Locate every Plasmodium falciparum-infected red blood cell.
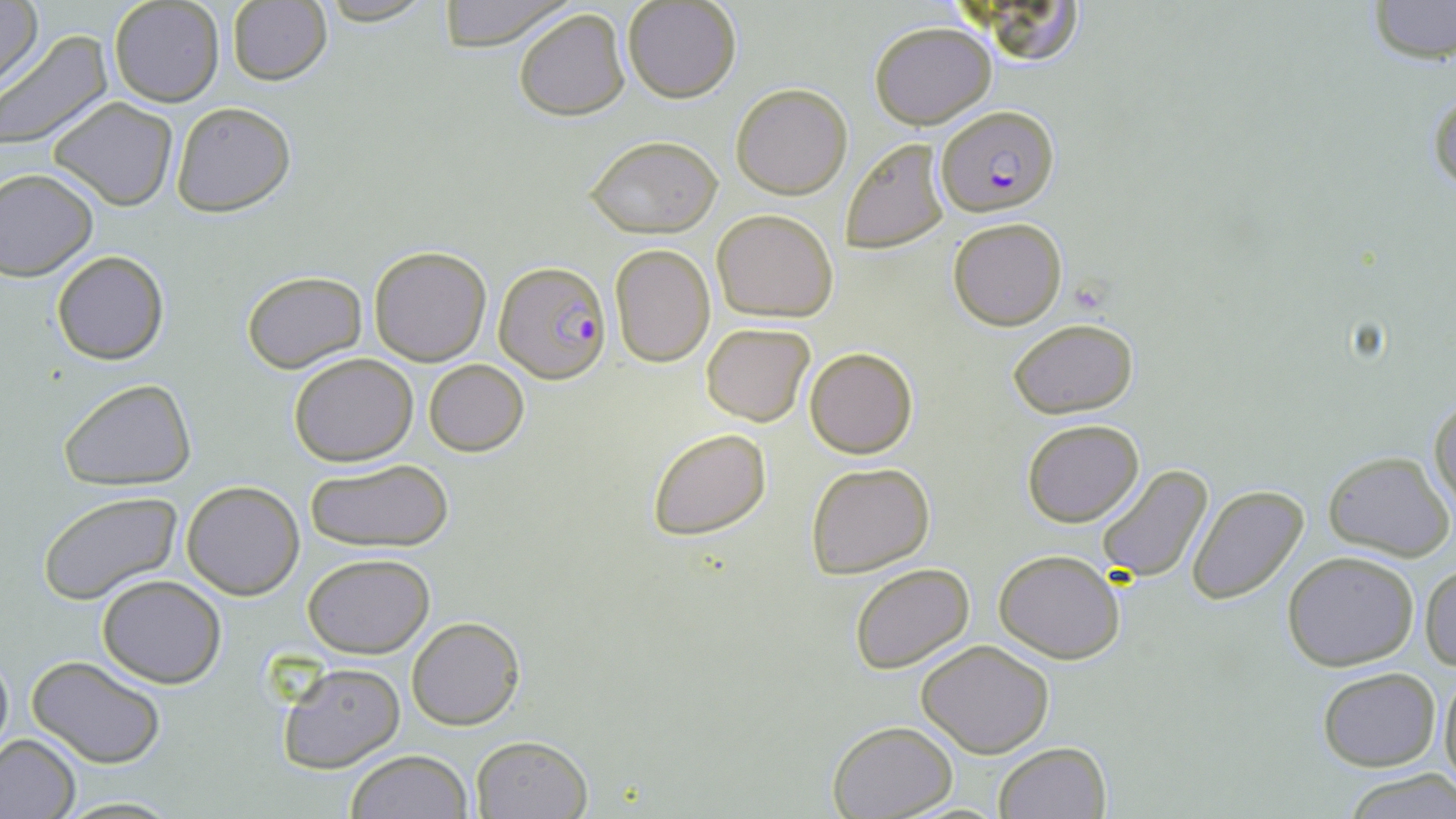

Approximate bounding boxes as named x1/y1/x2/y2 corners in pixels.
Plasmodium falciparum-infected red blood cells: (x1=935, y1=105, x2=1059, y2=216), (x1=495, y1=261, x2=613, y2=381).

{
  "slide_level_diagnosis": "Plasmodium falciparum",
  "preparation": "thin blood film",
  "magnification": "1000x",
  "uninfected_red_blood_cell_locations": "approximate bounding boxes as named x1/y1/x2/y2 corners in pixels: (x1=0, y1=0, x2=44, y2=92), (x1=622, y1=0, x2=742, y2=103), (x1=959, y1=0, x2=1090, y2=68), (x1=1366, y1=0, x2=1455, y2=65), (x1=107, y1=1, x2=225, y2=107), (x1=226, y1=1, x2=332, y2=87), (x1=435, y1=1, x2=571, y2=50), (x1=513, y1=7, x2=632, y2=120), (x1=869, y1=21, x2=996, y2=128), (x1=0, y1=30, x2=113, y2=151), (x1=1429, y1=80, x2=1456, y2=204), (x1=732, y1=83, x2=853, y2=199), (x1=47, y1=96, x2=177, y2=211), (x1=170, y1=101, x2=296, y2=218), (x1=583, y1=135, x2=722, y2=238), (x1=839, y1=137, x2=952, y2=254), (x1=0, y1=169, x2=98, y2=281), (x1=711, y1=208, x2=838, y2=322), (x1=948, y1=217, x2=1066, y2=330), (x1=610, y1=244, x2=715, y2=366), (x1=369, y1=245, x2=492, y2=366), (x1=52, y1=250, x2=169, y2=365), (x1=241, y1=270, x2=367, y2=374), (x1=1008, y1=318, x2=1138, y2=417), (x1=700, y1=322, x2=815, y2=427), (x1=804, y1=348, x2=917, y2=459), (x1=288, y1=353, x2=418, y2=465), (x1=424, y1=358, x2=530, y2=455), (x1=59, y1=379, x2=196, y2=490), (x1=1429, y1=394, x2=1455, y2=517), (x1=1021, y1=419, x2=1145, y2=528), (x1=647, y1=426, x2=771, y2=539), (x1=1323, y1=451, x2=1453, y2=561), (x1=305, y1=458, x2=455, y2=554), (x1=804, y1=461, x2=934, y2=577), (x1=1095, y1=464, x2=1214, y2=586), (x1=182, y1=481, x2=306, y2=600), (x1=1186, y1=485, x2=1308, y2=604), (x1=37, y1=492, x2=184, y2=607), (x1=993, y1=548, x2=1126, y2=664), (x1=1283, y1=550, x2=1418, y2=671), (x1=302, y1=552, x2=435, y2=658), (x1=848, y1=562, x2=976, y2=676), (x1=1422, y1=564, x2=1456, y2=671), (x1=97, y1=575, x2=227, y2=688), (x1=408, y1=618, x2=523, y2=730), (x1=917, y1=639, x2=1054, y2=758), (x1=0, y1=645, x2=13, y2=764), (x1=28, y1=655, x2=165, y2=768), (x1=276, y1=662, x2=405, y2=773), (x1=1438, y1=663, x2=1456, y2=795), (x1=1317, y1=667, x2=1441, y2=770), (x1=828, y1=720, x2=955, y2=818), (x1=0, y1=732, x2=81, y2=819), (x1=471, y1=734, x2=591, y2=818), (x1=994, y1=742, x2=1111, y2=819), (x1=346, y1=749, x2=471, y2=819), (x1=1345, y1=771, x2=1456, y2=818), (x1=57, y1=795, x2=186, y2=817)",
  "field_of_view": "one of a larger specimen",
  "stain": "May-Grünwald-Giemsa",
  "modality": "light microscopy",
  "image_size": "1456×819 pixels"
}